State the blood parasite species.
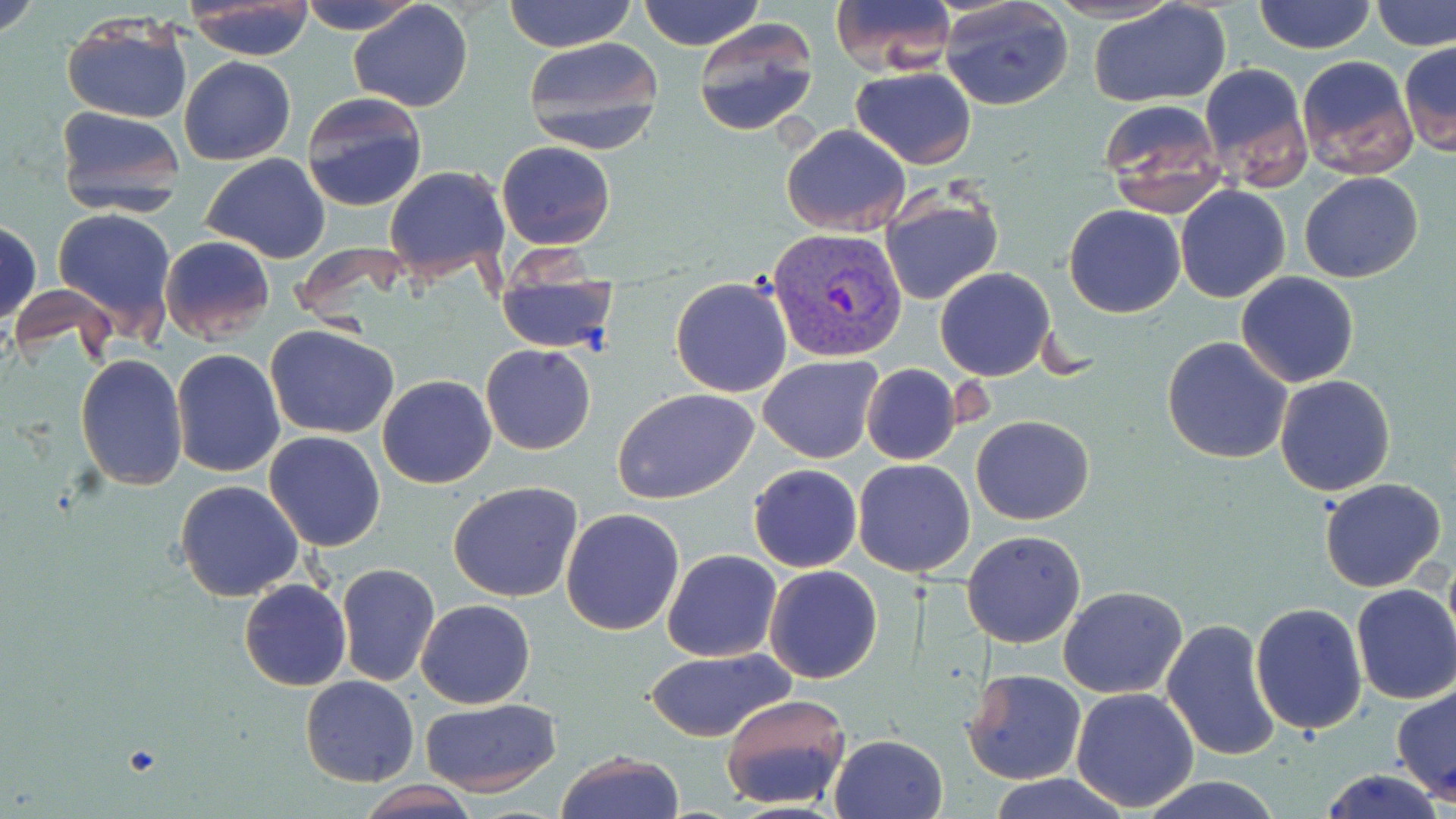

Plasmodium vivax.

Summary:
  - Coordinate format: approximate bounding boxes as named x1/y1/x2/y2 corners in pixels
  - Uninfected red blood cell locations: (x1=0, y1=0, x2=46, y2=42), (x1=302, y1=0, x2=420, y2=34), (x1=504, y1=0, x2=636, y2=51), (x1=637, y1=0, x2=764, y2=51), (x1=827, y1=0, x2=957, y2=75), (x1=940, y1=0, x2=1074, y2=110), (x1=1252, y1=0, x2=1377, y2=54), (x1=1373, y1=0, x2=1456, y2=52), (x1=1089, y1=1, x2=1234, y2=108), (x1=184, y1=2, x2=317, y2=60), (x1=348, y1=2, x2=473, y2=112), (x1=61, y1=13, x2=192, y2=124), (x1=692, y1=18, x2=819, y2=137), (x1=521, y1=35, x2=667, y2=153), (x1=1398, y1=42, x2=1456, y2=157), (x1=1295, y1=53, x2=1418, y2=181), (x1=178, y1=56, x2=297, y2=166), (x1=1197, y1=61, x2=1312, y2=190), (x1=851, y1=66, x2=976, y2=168), (x1=299, y1=90, x2=428, y2=213), (x1=1096, y1=98, x2=1228, y2=219), (x1=54, y1=105, x2=184, y2=217), (x1=780, y1=123, x2=912, y2=236), (x1=495, y1=140, x2=616, y2=250), (x1=201, y1=154, x2=330, y2=261), (x1=383, y1=164, x2=511, y2=280), (x1=1298, y1=171, x2=1423, y2=283), (x1=1175, y1=185, x2=1291, y2=302), (x1=878, y1=187, x2=1004, y2=307), (x1=1064, y1=203, x2=1185, y2=318), (x1=52, y1=207, x2=179, y2=335), (x1=0, y1=219, x2=42, y2=326), (x1=159, y1=235, x2=275, y2=347), (x1=493, y1=266, x2=620, y2=355), (x1=934, y1=267, x2=1056, y2=380), (x1=1235, y1=271, x2=1361, y2=387), (x1=669, y1=275, x2=793, y2=398), (x1=266, y1=325, x2=401, y2=439), (x1=1161, y1=336, x2=1294, y2=464), (x1=480, y1=343, x2=597, y2=455), (x1=170, y1=349, x2=286, y2=478), (x1=75, y1=354, x2=189, y2=491), (x1=758, y1=354, x2=882, y2=463), (x1=861, y1=364, x2=963, y2=466), (x1=377, y1=374, x2=497, y2=489), (x1=1274, y1=374, x2=1396, y2=496), (x1=611, y1=387, x2=760, y2=505), (x1=972, y1=414, x2=1094, y2=525), (x1=263, y1=432, x2=385, y2=551), (x1=851, y1=457, x2=976, y2=578), (x1=748, y1=463, x2=863, y2=572), (x1=1319, y1=477, x2=1446, y2=593), (x1=175, y1=480, x2=305, y2=603), (x1=447, y1=481, x2=585, y2=604), (x1=560, y1=508, x2=686, y2=636), (x1=961, y1=529, x2=1087, y2=648), (x1=662, y1=549, x2=782, y2=660), (x1=335, y1=563, x2=440, y2=687), (x1=764, y1=565, x2=883, y2=684), (x1=239, y1=579, x2=352, y2=691), (x1=1350, y1=583, x2=1456, y2=705), (x1=1058, y1=585, x2=1188, y2=697), (x1=416, y1=600, x2=536, y2=709), (x1=1248, y1=601, x2=1367, y2=735), (x1=1160, y1=618, x2=1283, y2=763), (x1=642, y1=647, x2=793, y2=744), (x1=963, y1=668, x2=1088, y2=785), (x1=299, y1=676, x2=418, y2=787), (x1=1392, y1=683, x2=1456, y2=807), (x1=1070, y1=688, x2=1201, y2=812), (x1=720, y1=692, x2=853, y2=812), (x1=420, y1=698, x2=562, y2=795), (x1=828, y1=734, x2=948, y2=819), (x1=556, y1=751, x2=684, y2=819), (x1=1317, y1=768, x2=1450, y2=819), (x1=983, y1=774, x2=1137, y2=819), (x1=1139, y1=775, x2=1285, y2=819), (x1=359, y1=781, x2=477, y2=818)
  - Plasmodium vivax-infected red blood cell locations: (x1=769, y1=225, x2=908, y2=362)
  - Magnification: 1000x
  - Stain: May-Grünwald-Giemsa
  - Modality: optical microscopy
  - Field of view: one of a larger specimen
  - Preparation: thin blood smear
  - Image size: 1456×819 pixels